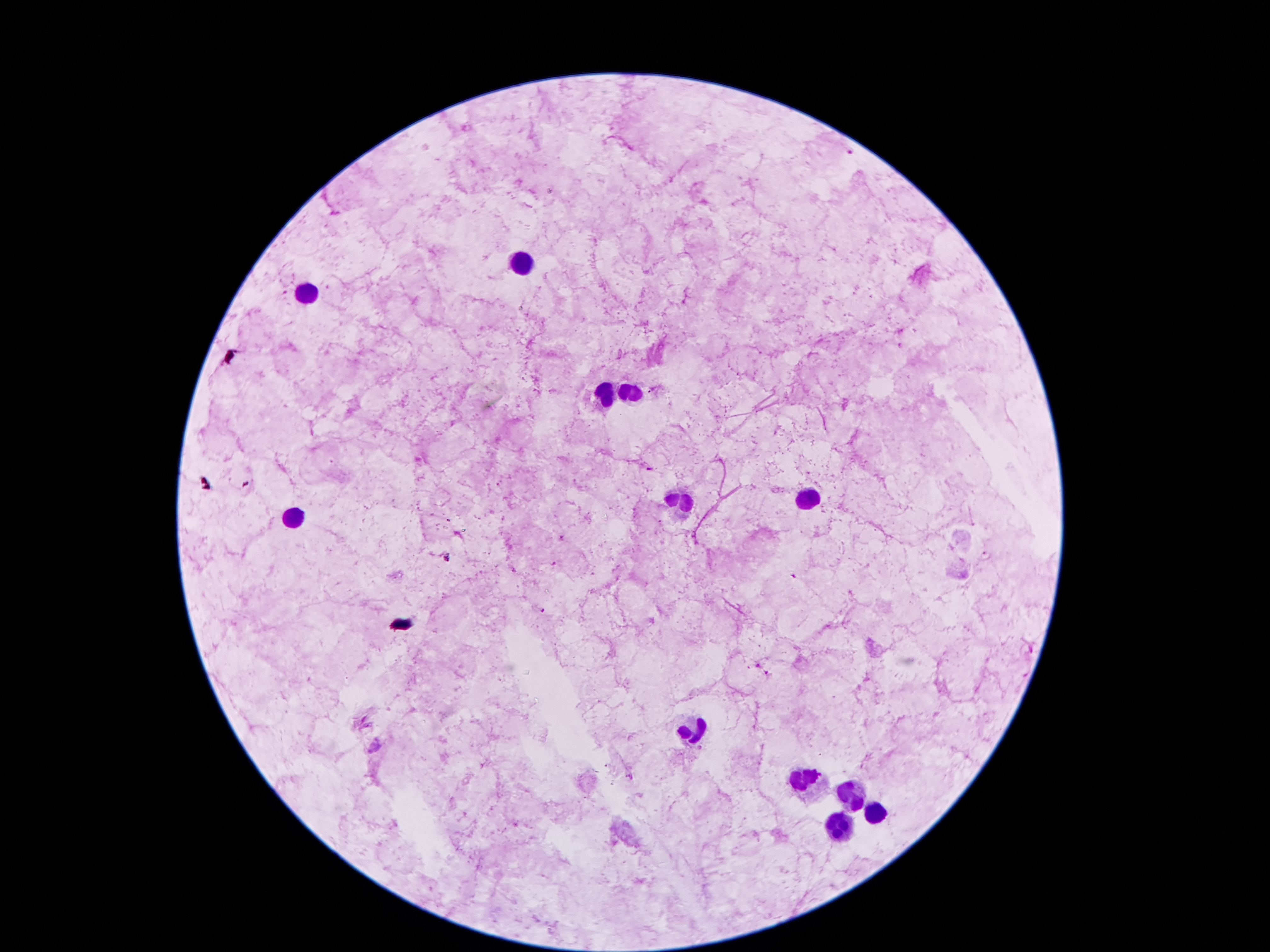
coordinate format = approximate centers as [x, y] in pixels
Plasmodium parasite locations = [849, 151], [652, 390], [648, 469], [561, 537], [987, 556], [447, 558], [554, 563], [541, 611], [757, 667], [768, 674]
leukocyte locations = [521, 260], [305, 294], [608, 392], [630, 392], [680, 499], [809, 499], [291, 512], [694, 728], [807, 781], [850, 796], [874, 814], [840, 828]
capture = smartphone through the microscope eyepiece
image size = 1270×952 pixels
preparation = thick peripheral-blood smear
patient malaria status = infected with Plasmodium falciparum
stain = Giemsa
field of view = single
magnification = 100x